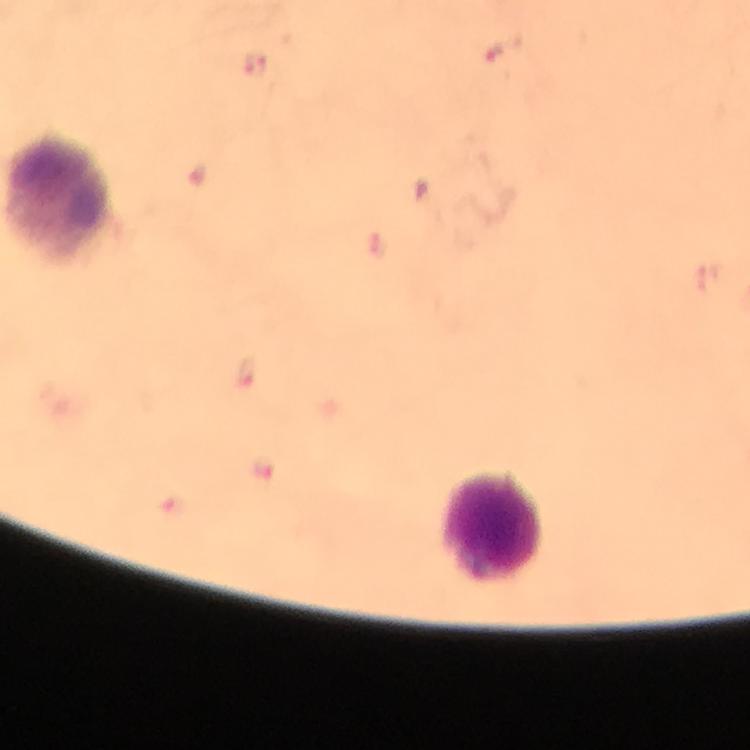

{
  "malaria_parasite_locations": "approximate centers as (x, y) in pixels: (503, 46), (255, 67), (246, 372)",
  "immersion_oil": "used",
  "capture": "smartphone mounted on the microscope",
  "context": "from a diagnostic examination for malaria",
  "image_size": "750×750 pixels",
  "preparation": "thick blood film",
  "magnification": "100x",
  "cropped_from": "one field of view",
  "leukocyte_locations": "approximate centers as (x, y) in pixels: (492, 527)",
  "stain": "Giemsa"
}